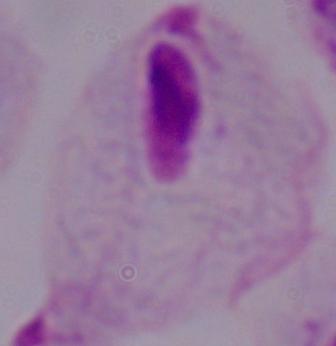
Summary:
  - Magnification: 1000x
  - Identification: trichomonad
  - Modality: photomicrograph